Identify the parasite.
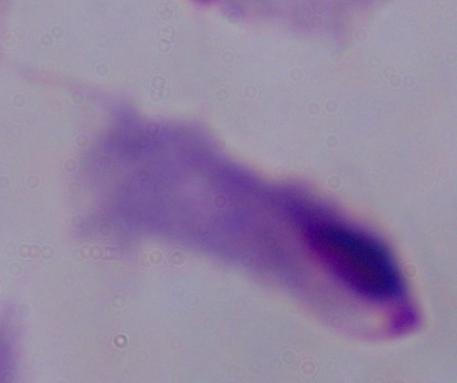
A trichomonad.

Summary:
  - Modality: micrograph
  - Magnification: 1000x